State the blood parasite species.
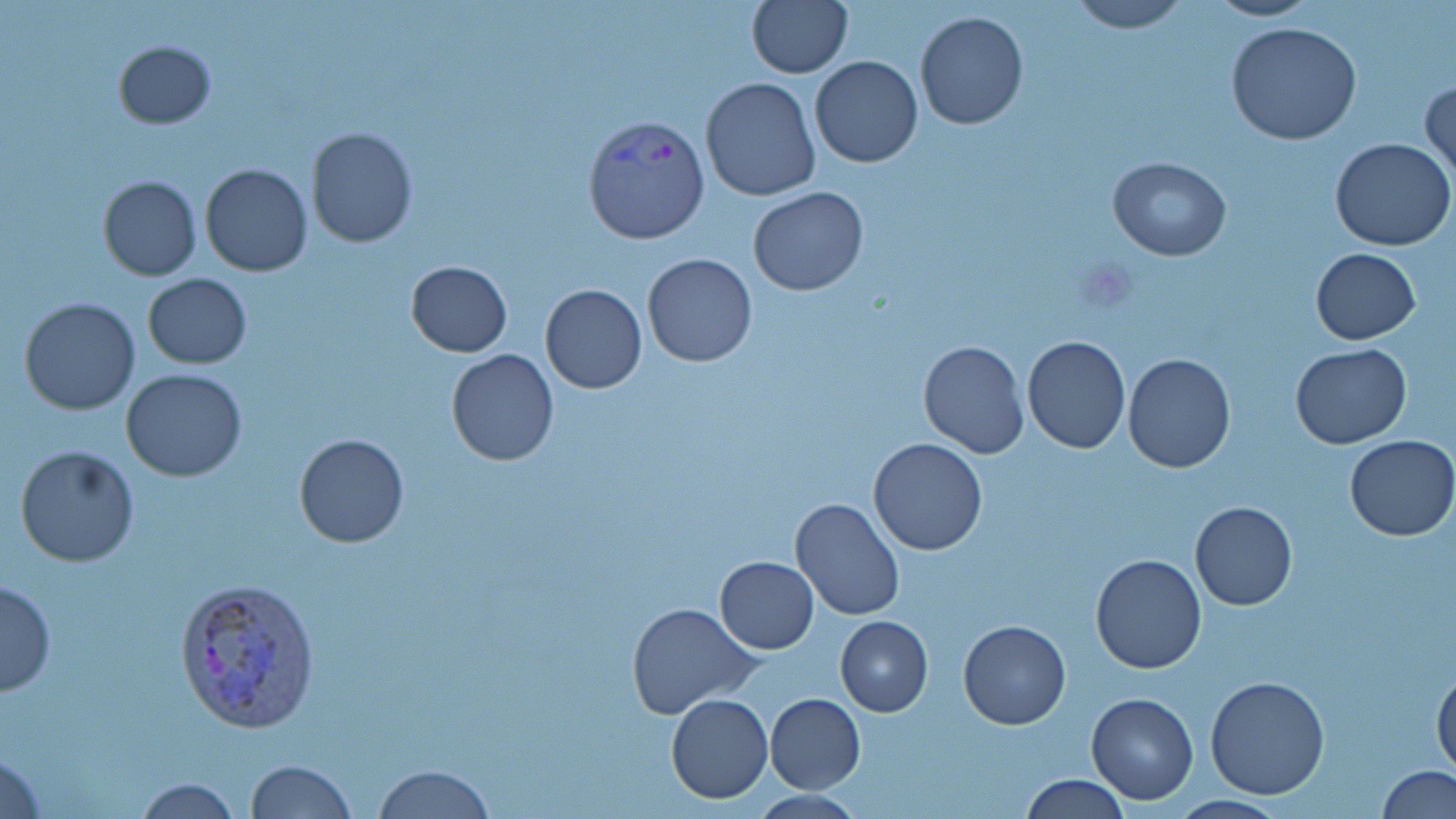
Plasmodium vivax.

Approximate bounding boxes as (x1,y1)-(x2,y2) corner pairs in pixels. Plasmodium vivax-infected red blood cell locations: (583,115)-(711,246), (175,578)-(322,732). Uninfected red blood cell locations: (746,0)-(852,79), (1069,0)-(1189,33), (1201,0)-(1322,22), (914,9)-(1029,131), (1225,21)-(1361,144), (113,39)-(216,128), (810,55)-(922,168), (700,77)-(820,202), (1420,78)-(1455,186), (305,127)-(417,249), (1332,138)-(1455,252), (1107,157)-(1231,260), (200,165)-(312,278), (97,175)-(202,280), (748,187)-(870,295), (1309,248)-(1421,345), (641,251)-(758,367), (405,260)-(512,357), (143,273)-(252,369), (540,284)-(647,395), (20,298)-(140,416), (1022,335)-(1131,454), (917,338)-(1029,459), (1290,344)-(1412,450), (446,348)-(559,466), (1121,353)-(1237,474), (120,367)-(248,482), (293,433)-(410,548), (1345,434)-(1456,542), (867,438)-(990,556), (15,445)-(139,567), (790,497)-(906,622), (1190,501)-(1297,611), (1090,554)-(1208,674), (715,556)-(819,654), (1,581)-(57,696), (626,601)-(758,718), (835,615)-(933,717), (958,620)-(1070,730), (1432,662)-(1455,776), (1205,676)-(1329,799), (1086,692)-(1198,804), (764,693)-(866,794), (666,694)-(774,803), (0,745)-(47,819), (245,759)-(357,818), (372,764)-(497,818), (1377,765)-(1455,819), (1020,773)-(1131,818), (131,777)-(245,817). Light microscopy. One field of a larger specimen. Image is 1456×819 pixels. Thin blood smear. Captured at 1000x magnification. May-Grünwald-Giemsa-stained preparation.